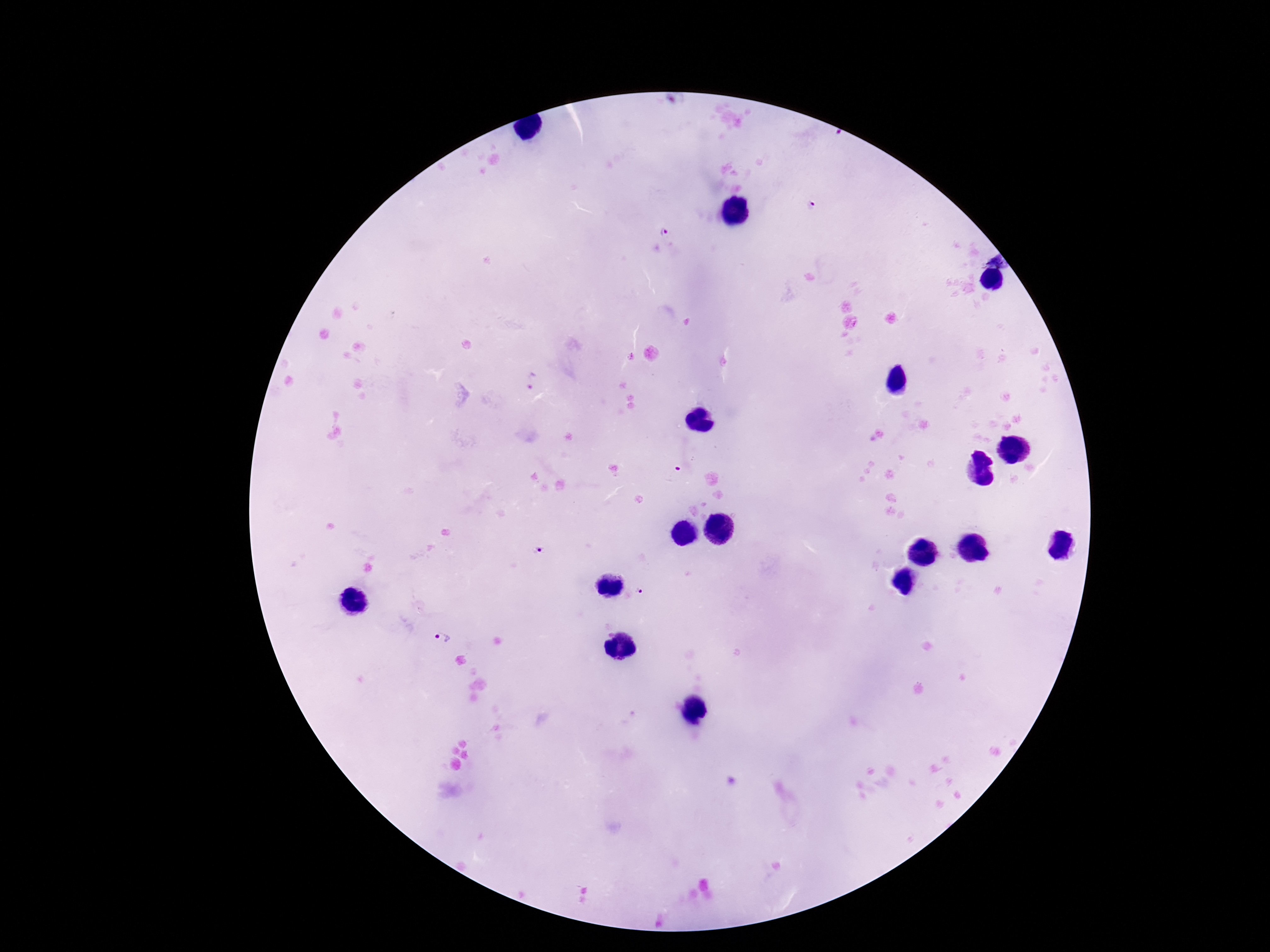
capture = smartphone camera through the microscope eyepiece
magnification = 100x
stain = Giemsa
preparation = thick peripheral-blood smear
image size = 1270×952 pixels
field of view = single
Plasmodium parasite locations = approximate centers as [x, y] in pixels: [812, 205], [665, 232], [534, 381], [540, 549], [639, 589], [443, 637]
patient malaria status = infected